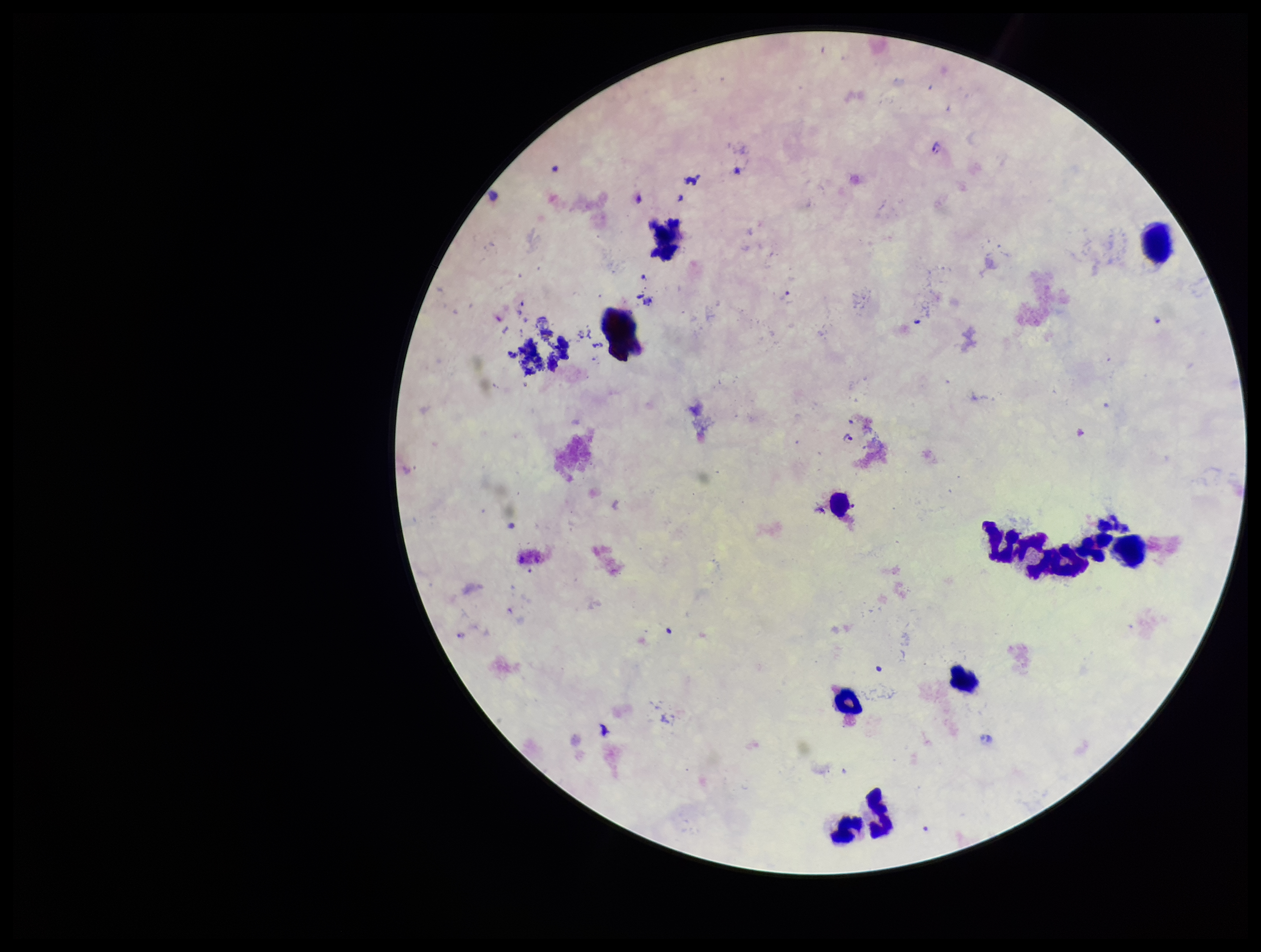

Plasmodium parasites = seen
capture = smartphone photograph through the microscope eyepiece
patient malaria status = infected
stain = Giemsa
parasite count = 2
species reported for this patient = Plasmodium falciparum
field of view = one from this slide
leukocyte count = 9
image size = 1261×952 pixels
preparation = thick blood smear